Report the malaria status of this cell.
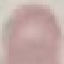

It is uninfected.

{
  "image_type": "cell patch, automatically extracted from a larger field of view and resized to 64 × 64 pixels",
  "preparation": "thin smear",
  "stain": "Giemsa",
  "capture": "smartphone through the microscope eyepiece"
}